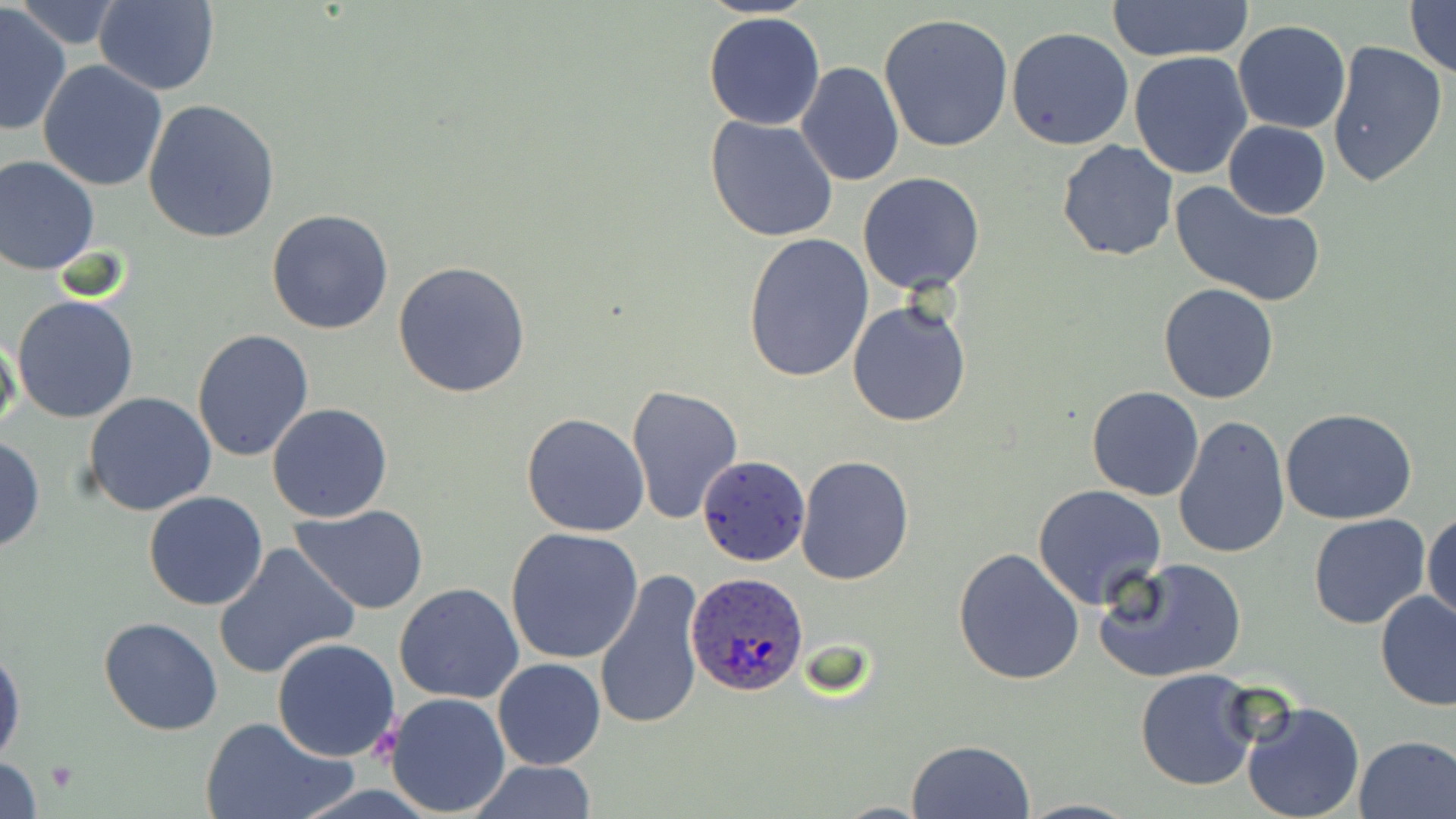

Summary:
  - Coordinate format: approximate bounding boxes as [x1, y1, x2, y2] in pixels
  - Uninfected red blood cell locations (subset): [1111, 0, 1252, 62], [1404, 0, 1455, 78], [92, 2, 221, 94], [0, 3, 73, 138], [20, 3, 119, 49], [702, 10, 827, 130], [878, 13, 1014, 151], [1232, 20, 1351, 134], [1006, 27, 1135, 150], [1327, 38, 1449, 188], [1129, 51, 1253, 179], [37, 61, 168, 191], [795, 61, 904, 185], [142, 98, 281, 243], [705, 116, 839, 243], [1223, 120, 1330, 218], [1056, 139, 1178, 262], [0, 153, 101, 275], [857, 172, 986, 295], [1169, 180, 1324, 306], [266, 208, 396, 334], [743, 231, 875, 383], [392, 261, 532, 399], [1158, 282, 1281, 403], [12, 295, 140, 424], [846, 298, 972, 429], [191, 328, 315, 464], [0, 330, 22, 444], [625, 384, 745, 524], [1086, 387, 1203, 501], [83, 392, 217, 517], [267, 402, 393, 523], [1280, 407, 1417, 524], [521, 412, 651, 538], [1172, 415, 1290, 561], [0, 435, 45, 554], [795, 455, 915, 585], [1031, 483, 1168, 610], [143, 491, 268, 611], [289, 505, 430, 614], [1423, 508, 1456, 629], [1308, 514, 1431, 630], [504, 528, 645, 665], [213, 543, 357, 681], [952, 547, 1086, 686], [1093, 555, 1248, 683], [593, 566, 709, 730], [1115, 568, 1254, 783], [394, 582, 525, 704], [1376, 592, 1456, 711], [98, 616, 222, 736], [272, 637, 401, 760], [0, 638, 25, 770], [493, 658, 606, 770], [1134, 669, 1261, 793], [383, 692, 512, 815], [1239, 699, 1366, 819], [202, 715, 352, 819], [1353, 734, 1456, 818], [906, 738, 1035, 819], [0, 755, 43, 818], [464, 761, 600, 817]
  - Plasmodium ovale-infected red blood cell locations (subset): [687, 574, 807, 698]
  - Platelet locations: [369, 725, 403, 756], [47, 761, 77, 792]
  - Slide-level diagnosis: Plasmodium ovale
  - Stain: May-Grünwald-Giemsa
  - Magnification: 1000x
  - Modality: light microscopy
  - Field of view: one of a larger specimen
  - Image size: 1456×819 pixels
  - Preparation: thin blood film